Classify this cell by malaria status.
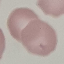
Uninfected.

Photographed with a smartphone camera at the microscope eyepiece. Thin blood smear. Cell patch, automatically extracted from a larger field of view and resized to 64 × 64 pixels. Giemsa-stained preparation.